Classify this cell by malaria status.
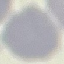
Uninfected.

Summary:
  - Capture: smartphone camera at the microscope eyepiece
  - Stain: Giemsa
  - Preparation: thin blood smear
  - Image type: automatically extracted cell patch, resized to 64 × 64 pixels